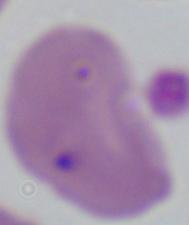
magnification = 1000x
modality = micrograph
identification = Babesia